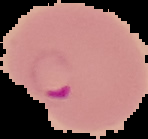
Summary:
  - Image type: segmented cell region with the area outside set to black
  - Image size: 148×139 pixels
  - Preparation: thin blood smear
  - Result: malaria parasites identified